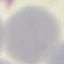

Summary:
  - Malaria status: uninfected
  - Stain: Giemsa
  - Preparation: thin blood film
  - Image type: automatically extracted cell patch, resized to 64 × 64 pixels
  - Capture: smartphone through the microscope eyepiece